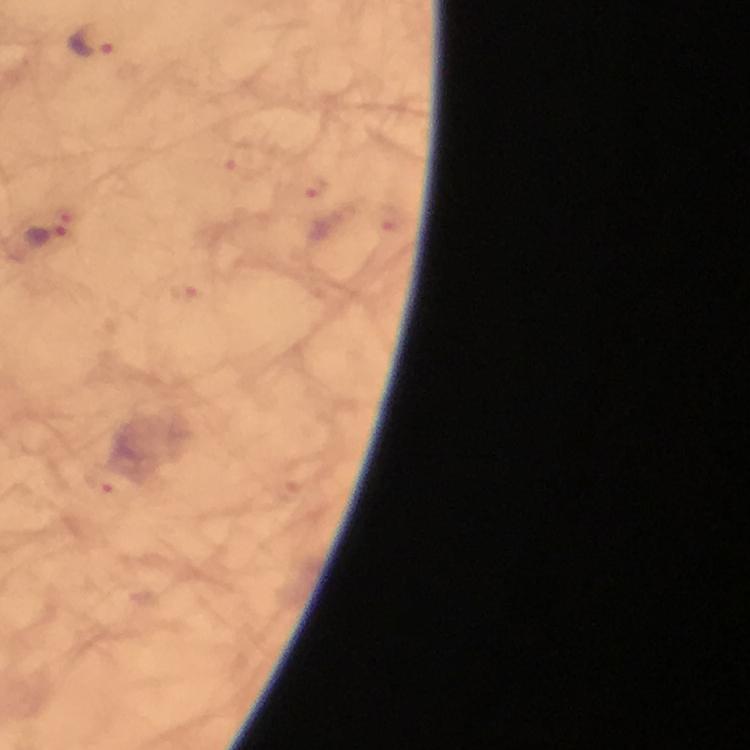

image size = 750×750 pixels
preparation = thick blood film
capture = smartphone mounted on the microscope
magnification = 100x
stain = Giemsa
context = from a diagnostic examination for malaria
immersion oil = applied
Plasmodium parasite locations = approximate object centers, in pixels from the top-left corner: (x=89, y=39), (x=239, y=160), (x=317, y=187), (x=392, y=222), (x=44, y=238), (x=185, y=292), (x=110, y=479)
cropped from = one field of view